Name the blood parasite species.
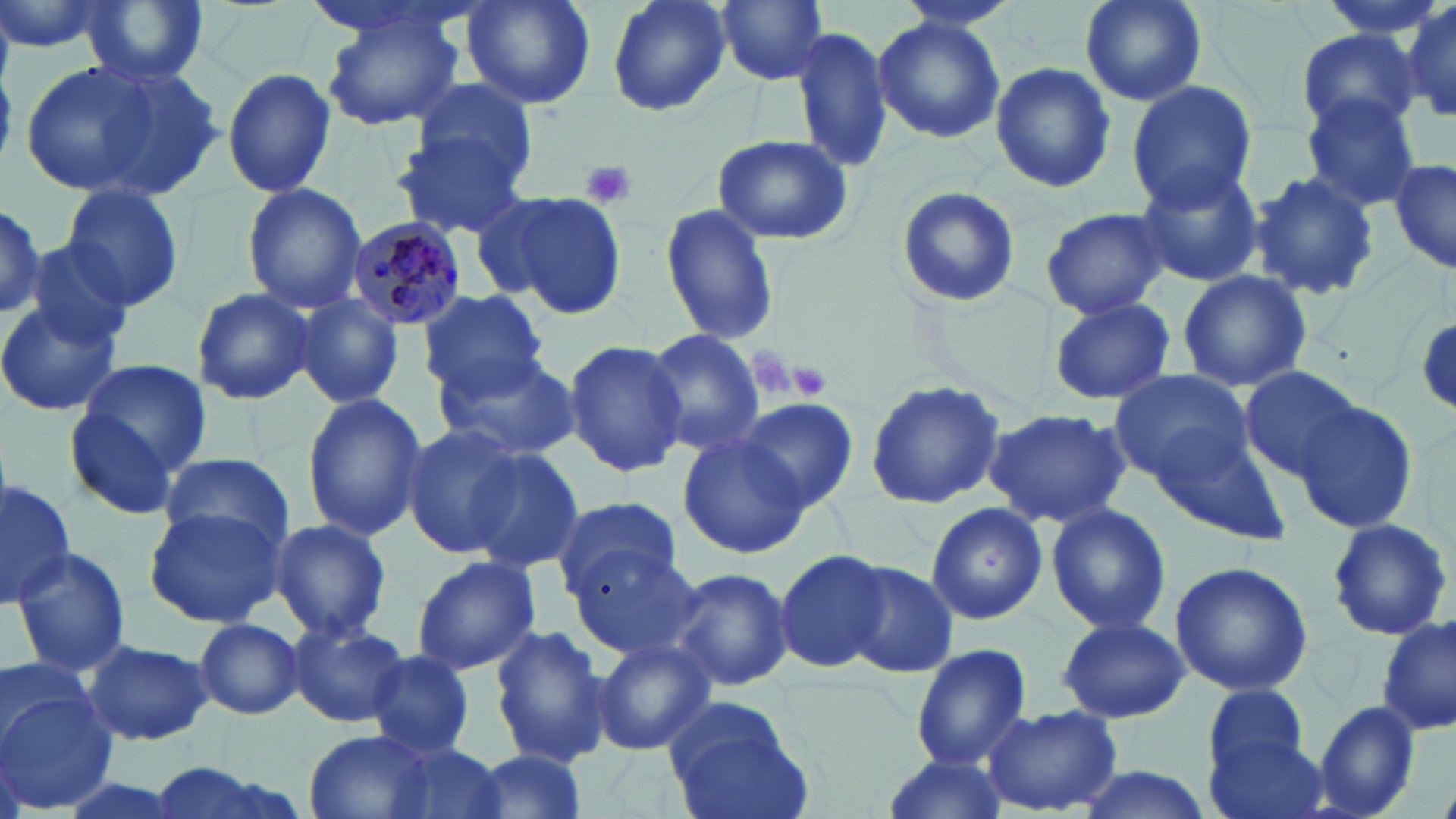

Plasmodium malariae.

Approximate bounding boxes as (x1,y1)-(x2,y2) corner pairs in pixels. Platelet locations: (579,159)-(637,210), (746,348)-(797,401), (783,361)-(831,401). Plasmodium malariae-infected red blood cell locations: (342,216)-(466,331). Uninfected red blood cell locations: (0,0)-(109,56), (77,0)-(211,88), (462,0)-(595,111), (605,0)-(731,118), (715,0)-(831,84), (890,0)-(1027,32), (1078,0)-(1205,108), (1399,0)-(1455,125), (323,11)-(466,130), (872,16)-(1004,143), (791,24)-(895,174), (1293,30)-(1420,134), (989,61)-(1118,193), (20,62)-(163,196), (71,63)-(225,204), (222,66)-(337,199), (408,80)-(542,188), (1125,80)-(1258,212), (1300,97)-(1423,210), (394,133)-(529,239), (713,135)-(851,245), (1390,159)-(1455,275), (1134,164)-(1264,287), (1247,170)-(1381,303), (240,182)-(367,314), (61,183)-(185,313), (896,186)-(1022,309), (465,191)-(569,300), (487,191)-(627,319), (0,198)-(48,320), (659,203)-(780,347), (1041,208)-(1172,318), (25,240)-(137,346), (1176,271)-(1312,393), (191,287)-(315,405), (419,288)-(548,399), (294,294)-(404,408), (1048,296)-(1175,406), (0,297)-(123,418), (1413,315)-(1456,410), (644,330)-(768,456), (563,339)-(689,475), (435,350)-(582,461), (75,358)-(214,476), (1238,366)-(1362,480), (1108,368)-(1253,485), (864,381)-(1004,507), (300,391)-(426,542), (1295,395)-(1420,536), (731,398)-(859,515), (66,407)-(176,521), (983,407)-(1132,529), (1147,413)-(1294,544), (400,425)-(526,560), (677,432)-(811,558), (460,448)-(585,574), (158,452)-(295,550), (0,476)-(76,610), (551,495)-(687,597), (927,500)-(1050,626), (1043,502)-(1171,636), (144,506)-(287,628), (269,517)-(393,643), (1324,517)-(1452,642), (566,544)-(704,660), (10,548)-(134,678), (773,550)-(888,674), (410,555)-(543,676), (838,558)-(961,678), (1170,561)-(1313,695), (662,566)-(796,693), (1377,615)-(1453,739), (1057,616)-(1188,723), (193,617)-(304,719), (286,619)-(410,728), (490,624)-(615,768), (82,638)-(213,746), (590,638)-(716,755), (910,643)-(1033,770), (367,650)-(476,759), (0,653)-(95,750), (1204,684)-(1313,782), (0,694)-(115,814), (662,699)-(812,817), (1312,700)-(1422,819), (984,704)-(1123,816), (1203,723)-(1329,819), (304,729)-(445,819), (372,741)-(510,819), (465,751)-(591,818), (877,753)-(1008,819), (142,759)-(304,819), (1068,766)-(1216,819). Thin blood film. May-Grünwald-Giemsa-stained preparation. One field of a larger specimen. Light microscopy. Image is 1456×819 pixels. Captured at 1000x magnification.